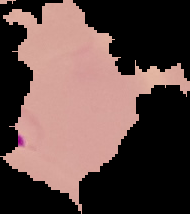
image size = 190×214 pixels
preparation = thin blood film
image type = cell region segmented out of the field of view; surrounding area masked to black
result = Plasmodium parasites detected